Assess the morphology of the red blood cells.
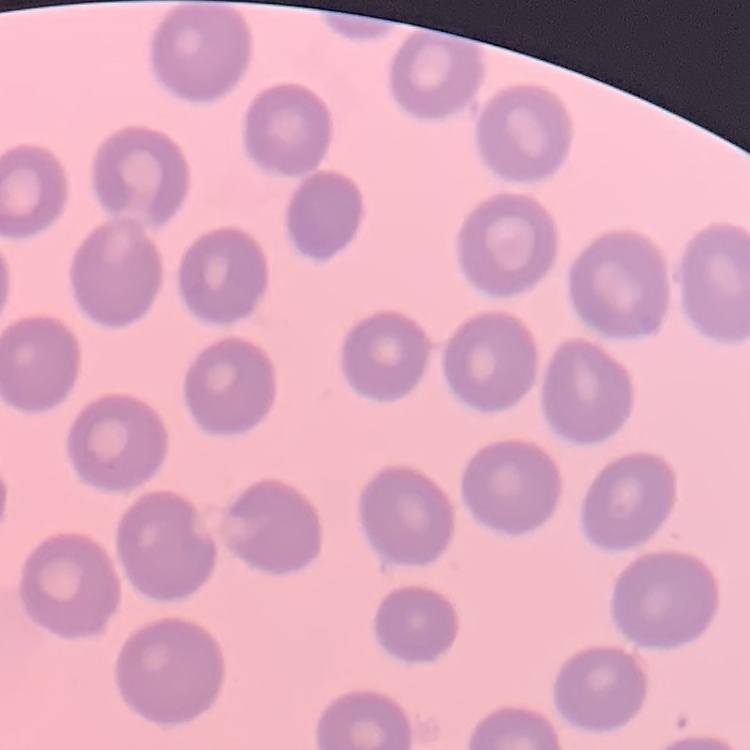
They show no rouleaux formation.

Summary:
  - Image type: square crop of a larger photomicrograph
  - Stain: Field's or Giemsa
  - Preparation: thin blood smear